Assess the morphology of the red blood cells.
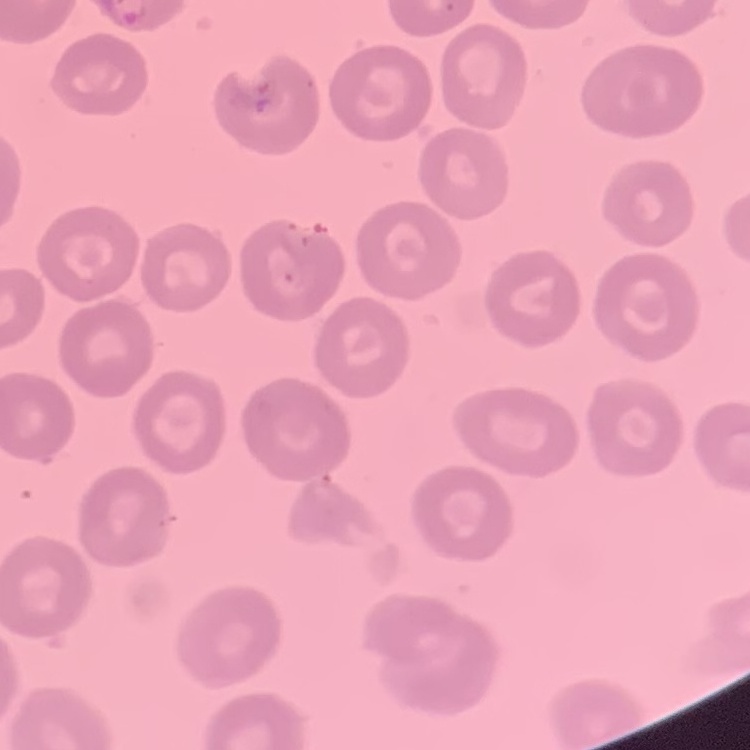

They show no rouleaux formation.

Summary:
  - Preparation: thin blood smear
  - Image type: one tile cut from a larger photomicrograph
  - Stain: Field's or Giemsa